State the blood parasite species.
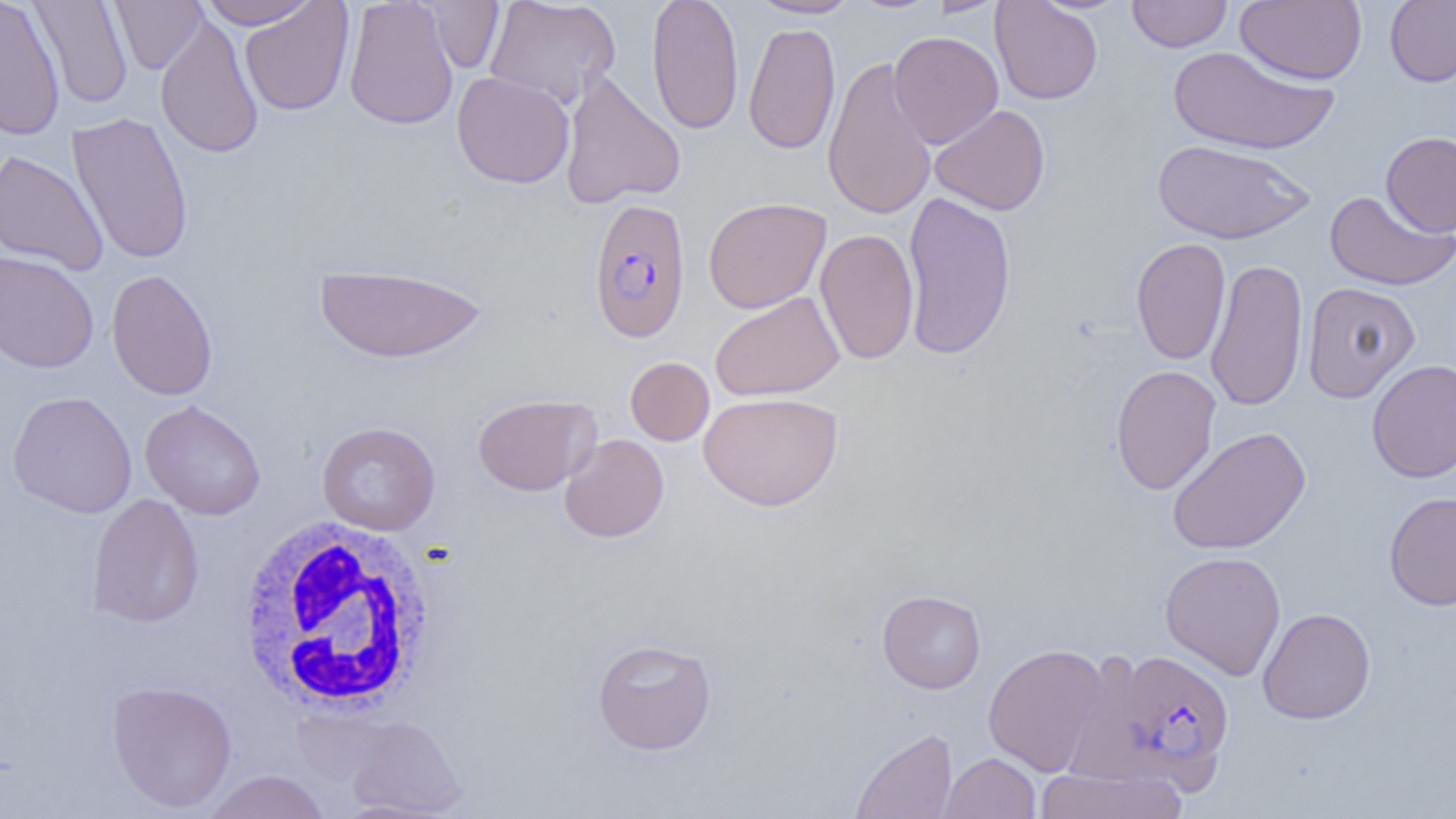
Plasmodium falciparum.

Summary:
  - Coordinate format: approximate bounding boxes as named x1/y1/x2/y2 corners in pixels
  - White blood cell locations: (x1=235, y1=514, x2=441, y2=716)
  - Plasmodium falciparum-infected red blood cell locations: (x1=587, y1=197, x2=691, y2=343), (x1=1088, y1=647, x2=1237, y2=794)
  - Uninfected red blood cell locations: (x1=0, y1=0, x2=65, y2=141), (x1=28, y1=0, x2=133, y2=109), (x1=197, y1=0, x2=320, y2=29), (x1=343, y1=0, x2=459, y2=130), (x1=484, y1=0, x2=621, y2=109), (x1=646, y1=0, x2=744, y2=136), (x1=747, y1=0, x2=861, y2=19), (x1=990, y1=0, x2=1103, y2=105), (x1=1127, y1=0, x2=1232, y2=52), (x1=1235, y1=0, x2=1366, y2=85), (x1=1385, y1=0, x2=1456, y2=87), (x1=110, y1=1, x2=206, y2=74), (x1=422, y1=1, x2=505, y2=73), (x1=240, y1=2, x2=354, y2=116), (x1=155, y1=13, x2=264, y2=159), (x1=743, y1=21, x2=841, y2=155), (x1=888, y1=31, x2=1004, y2=149), (x1=1167, y1=44, x2=1338, y2=156), (x1=822, y1=55, x2=938, y2=221), (x1=559, y1=70, x2=686, y2=209), (x1=451, y1=71, x2=575, y2=188), (x1=929, y1=104, x2=1050, y2=216), (x1=67, y1=112, x2=194, y2=265), (x1=1380, y1=131, x2=1456, y2=237), (x1=1152, y1=139, x2=1315, y2=245), (x1=0, y1=149, x2=109, y2=276), (x1=901, y1=190, x2=1017, y2=362), (x1=1324, y1=190, x2=1454, y2=290), (x1=703, y1=196, x2=831, y2=314), (x1=815, y1=227, x2=919, y2=365), (x1=1131, y1=237, x2=1230, y2=366), (x1=0, y1=250, x2=99, y2=374), (x1=1205, y1=257, x2=1308, y2=411), (x1=2, y1=260, x2=219, y2=382), (x1=313, y1=263, x2=490, y2=364), (x1=106, y1=268, x2=218, y2=401), (x1=1302, y1=282, x2=1420, y2=402), (x1=710, y1=291, x2=844, y2=402), (x1=625, y1=356, x2=714, y2=446), (x1=1367, y1=360, x2=1456, y2=483), (x1=1110, y1=364, x2=1222, y2=495), (x1=7, y1=390, x2=137, y2=519), (x1=699, y1=391, x2=843, y2=511), (x1=472, y1=393, x2=600, y2=496), (x1=140, y1=400, x2=266, y2=520), (x1=316, y1=421, x2=441, y2=535), (x1=1167, y1=426, x2=1311, y2=555), (x1=559, y1=434, x2=669, y2=543), (x1=1384, y1=491, x2=1456, y2=610), (x1=86, y1=493, x2=204, y2=628), (x1=1160, y1=550, x2=1286, y2=680), (x1=877, y1=589, x2=986, y2=693), (x1=1257, y1=607, x2=1376, y2=725), (x1=591, y1=638, x2=717, y2=755), (x1=983, y1=643, x2=1110, y2=776), (x1=106, y1=680, x2=237, y2=813), (x1=345, y1=716, x2=466, y2=816), (x1=849, y1=728, x2=957, y2=818), (x1=939, y1=752, x2=1041, y2=818), (x1=1036, y1=766, x2=1187, y2=818), (x1=202, y1=770, x2=331, y2=819)
  - Preparation: thin blood film
  - Magnification: 1000x
  - Image size: 1456×819 pixels
  - Field of view: single
  - Modality: light microscopy